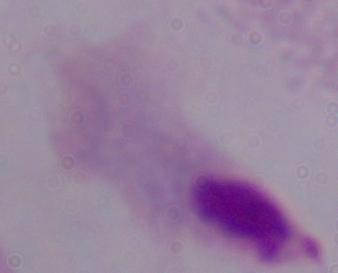
Summary:
  - Modality: micrograph
  - Magnification: 1000x
  - Identification: trichomonad